Assess this cell for malaria.
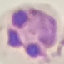
It is parasitized.

image type = cell patch, automatically extracted from a larger field of view and resized to 64 × 64 pixels
capture = smartphone camera at the microscope eyepiece
preparation = thin smear
stain = Giemsa